Assess this cell for malaria.
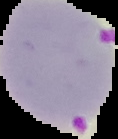
It is parasitized.

Image is 118×139 pixels. From a thin blood film. Cell region segmented out of the field of view; the surrounding area is masked to black.